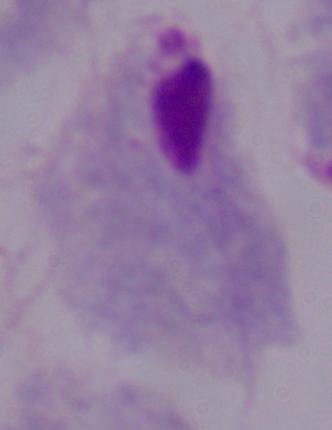

1000x magnification. A trichomonad is shown. Micrograph.